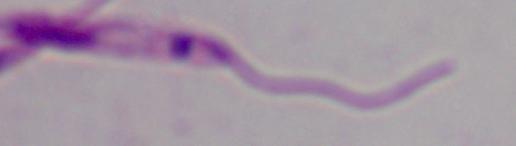
magnification = 1000x
identification = Leishmania
modality = micrograph